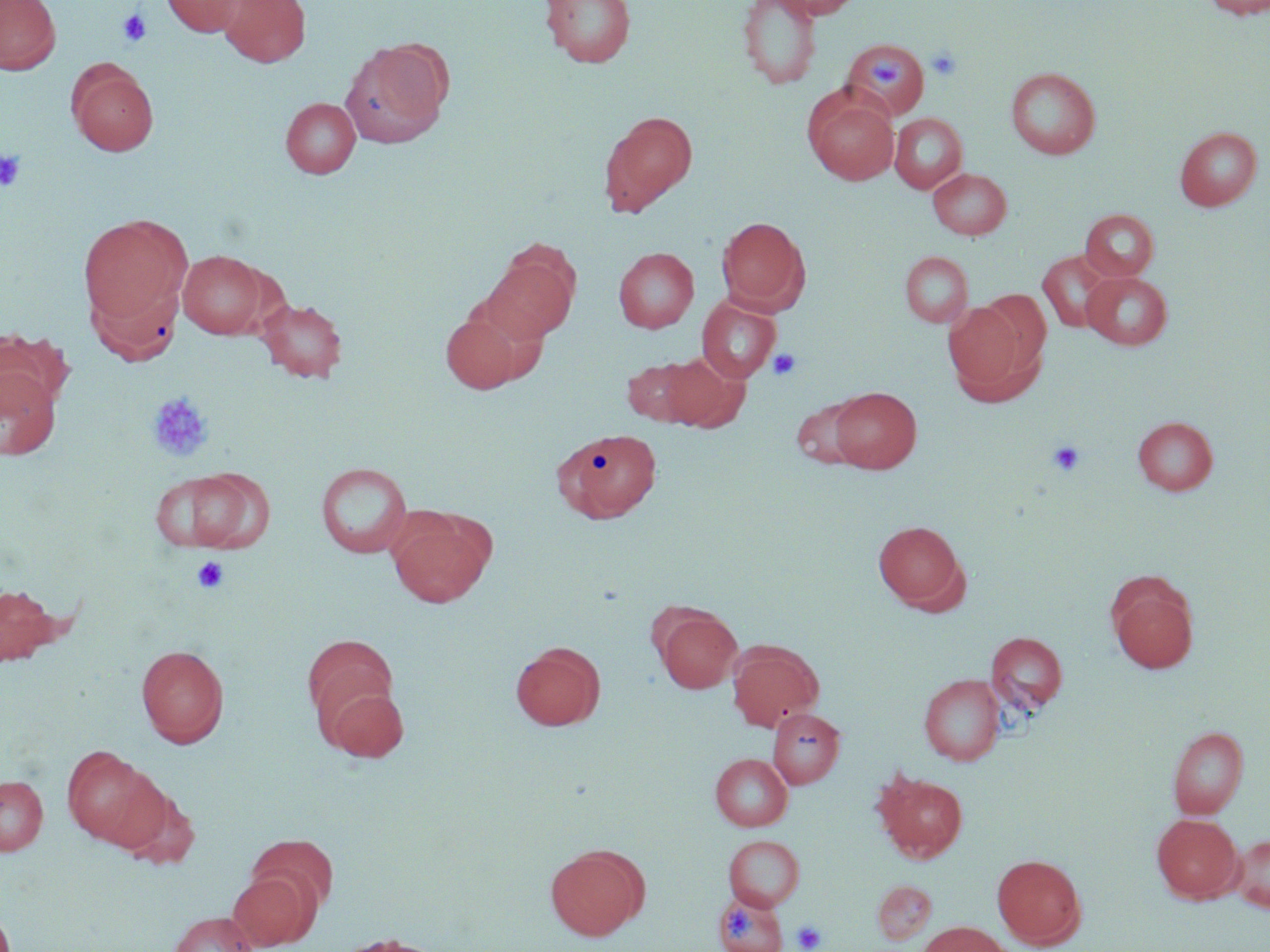

Approximate bounding boxes as named x1/y1/x2/y2 corners in pixels. Platelet locations: (x1=117, y1=8, x2=153, y2=47), (x1=927, y1=46, x2=963, y2=81), (x1=867, y1=54, x2=907, y2=88), (x1=0, y1=150, x2=26, y2=192), (x1=768, y1=348, x2=802, y2=380), (x1=147, y1=392, x2=214, y2=462), (x1=1048, y1=440, x2=1085, y2=476), (x1=191, y1=556, x2=229, y2=594), (x1=727, y1=908, x2=754, y2=939), (x1=792, y1=919, x2=827, y2=951). Uninfected red blood cell locations: (x1=0, y1=0, x2=61, y2=74), (x1=162, y1=0, x2=247, y2=37), (x1=219, y1=0, x2=310, y2=67), (x1=540, y1=0, x2=636, y2=68), (x1=737, y1=0, x2=823, y2=89), (x1=772, y1=0, x2=863, y2=20), (x1=1200, y1=0, x2=1270, y2=19), (x1=842, y1=37, x2=929, y2=121), (x1=341, y1=40, x2=450, y2=147), (x1=67, y1=61, x2=158, y2=157), (x1=1005, y1=67, x2=1101, y2=159), (x1=803, y1=89, x2=899, y2=185), (x1=281, y1=97, x2=361, y2=178), (x1=598, y1=110, x2=698, y2=216), (x1=889, y1=113, x2=967, y2=193), (x1=1174, y1=126, x2=1263, y2=211), (x1=928, y1=167, x2=1012, y2=239), (x1=1080, y1=209, x2=1159, y2=281), (x1=78, y1=214, x2=191, y2=326), (x1=716, y1=216, x2=809, y2=311), (x1=482, y1=247, x2=579, y2=343), (x1=613, y1=247, x2=699, y2=333), (x1=177, y1=250, x2=269, y2=339), (x1=1038, y1=250, x2=1114, y2=333), (x1=900, y1=251, x2=973, y2=328), (x1=1082, y1=271, x2=1172, y2=349), (x1=87, y1=274, x2=185, y2=366), (x1=972, y1=289, x2=1051, y2=375), (x1=255, y1=297, x2=348, y2=383), (x1=696, y1=297, x2=781, y2=382), (x1=943, y1=301, x2=1035, y2=398), (x1=439, y1=308, x2=536, y2=393), (x1=0, y1=329, x2=71, y2=416), (x1=660, y1=352, x2=748, y2=432), (x1=621, y1=358, x2=703, y2=426), (x1=0, y1=366, x2=61, y2=460), (x1=828, y1=386, x2=922, y2=473), (x1=791, y1=395, x2=873, y2=470), (x1=1133, y1=416, x2=1218, y2=495), (x1=553, y1=428, x2=662, y2=522), (x1=315, y1=462, x2=413, y2=559), (x1=150, y1=468, x2=272, y2=553), (x1=387, y1=510, x2=492, y2=607), (x1=873, y1=520, x2=967, y2=611), (x1=1106, y1=573, x2=1200, y2=674), (x1=0, y1=582, x2=63, y2=666), (x1=654, y1=608, x2=742, y2=693), (x1=986, y1=631, x2=1068, y2=714), (x1=303, y1=635, x2=401, y2=744), (x1=727, y1=640, x2=824, y2=731), (x1=511, y1=642, x2=605, y2=730), (x1=136, y1=643, x2=229, y2=748), (x1=919, y1=674, x2=1005, y2=765), (x1=318, y1=678, x2=410, y2=763), (x1=768, y1=708, x2=845, y2=788), (x1=1168, y1=726, x2=1249, y2=818), (x1=62, y1=746, x2=165, y2=849), (x1=710, y1=753, x2=793, y2=830), (x1=873, y1=770, x2=968, y2=861), (x1=0, y1=775, x2=48, y2=855), (x1=111, y1=779, x2=198, y2=868), (x1=1151, y1=813, x2=1242, y2=903), (x1=245, y1=834, x2=339, y2=919), (x1=1230, y1=834, x2=1270, y2=912), (x1=724, y1=835, x2=805, y2=910), (x1=545, y1=843, x2=648, y2=940), (x1=992, y1=854, x2=1087, y2=949), (x1=228, y1=870, x2=316, y2=950), (x1=872, y1=880, x2=937, y2=945), (x1=713, y1=892, x2=787, y2=952), (x1=169, y1=911, x2=258, y2=952), (x1=917, y1=922, x2=1011, y2=952), (x1=333, y1=933, x2=447, y2=952). Slide-level diagnosis: no evidence of blood parasites. Light microscopy. Thin blood smear. May-Grünwald-Giemsa stain. Image is 1270×952 pixels. One field of a larger specimen. Captured at 1000x magnification.